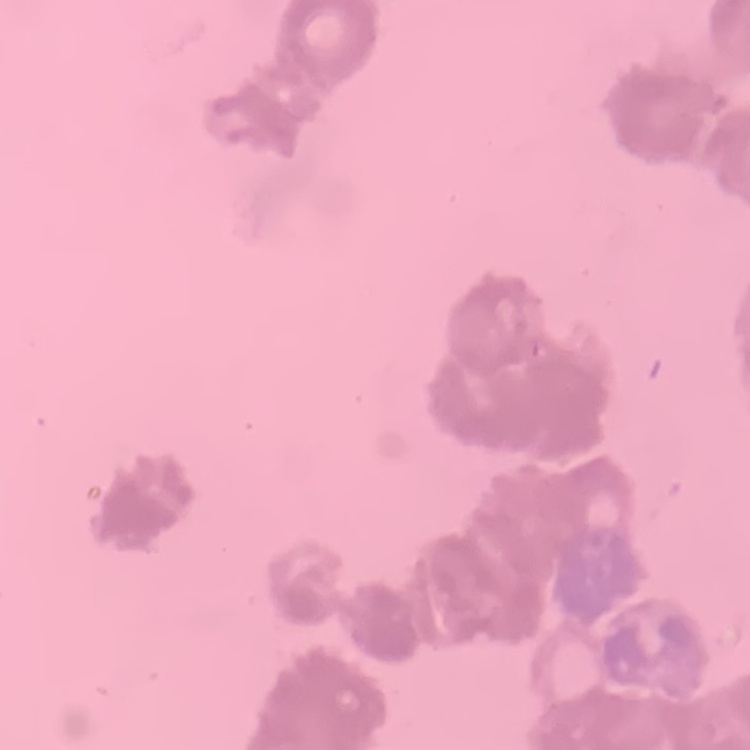

Summary:
  - Erythrocyte morphology: rouleaux formation
  - Image type: one tile cut from a larger photomicrograph
  - Stain: Field's or Giemsa
  - Preparation: thin peripheral smear